Give the extent of all Trypanosoma brucei.
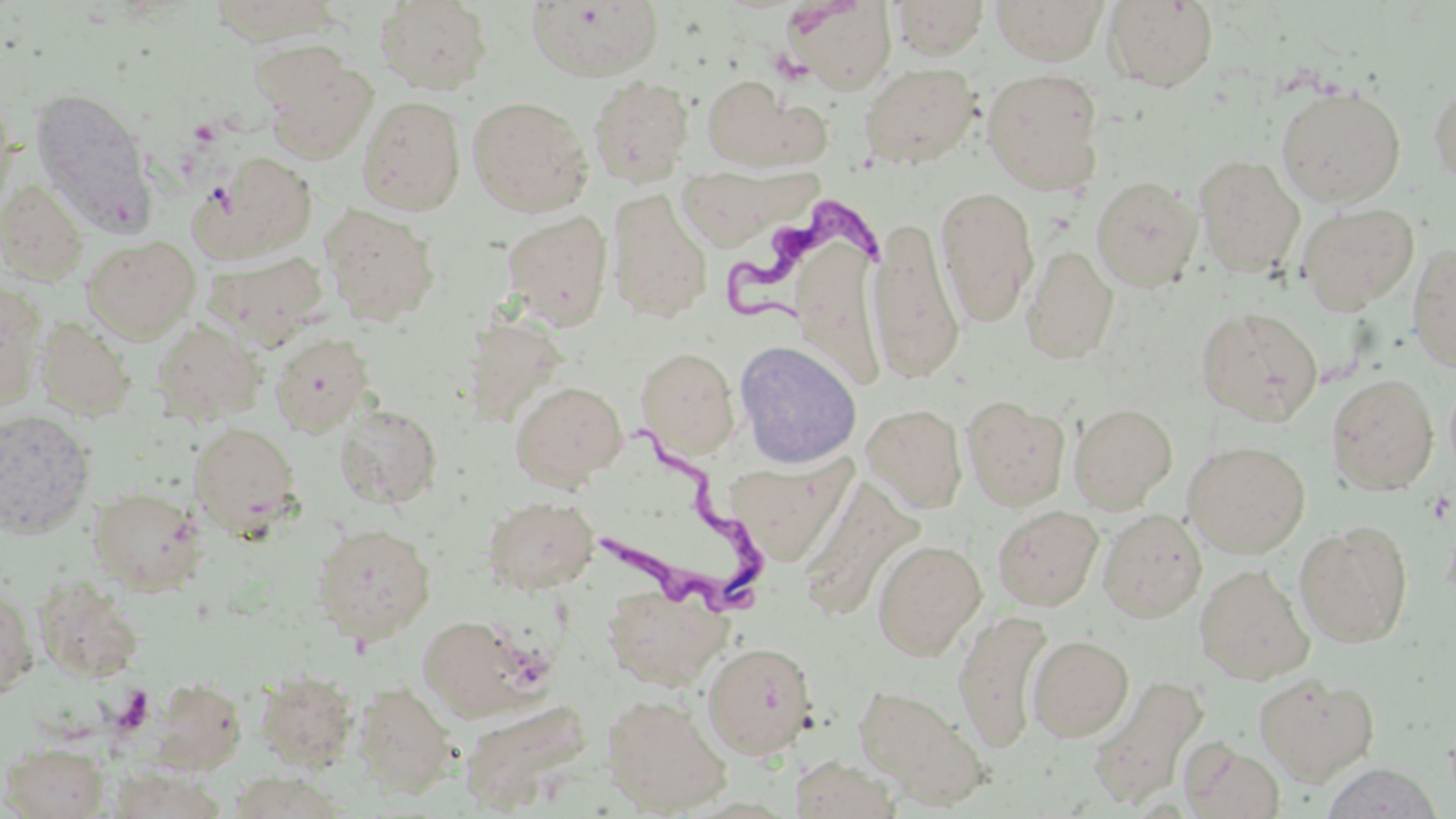
Approximate bounding boxes as named x1/y1/x2/y2 corners in pixels.
Trypanosoma brucei: (x1=719, y1=196, x2=880, y2=326), (x1=591, y1=423, x2=774, y2=619).

Uninfected red blood cell locations: (x1=206, y1=0, x2=344, y2=45), (x1=787, y1=0, x2=896, y2=94), (x1=991, y1=0, x2=1108, y2=64), (x1=375, y1=1, x2=493, y2=93), (x1=527, y1=1, x2=664, y2=82), (x1=890, y1=1, x2=989, y2=60), (x1=1104, y1=1, x2=1219, y2=91), (x1=258, y1=47, x2=378, y2=161), (x1=858, y1=62, x2=982, y2=170), (x1=982, y1=69, x2=1106, y2=196), (x1=588, y1=75, x2=695, y2=186), (x1=700, y1=75, x2=826, y2=172), (x1=1428, y1=80, x2=1456, y2=189), (x1=0, y1=85, x2=18, y2=212), (x1=1274, y1=85, x2=1406, y2=206), (x1=29, y1=86, x2=154, y2=230), (x1=357, y1=95, x2=467, y2=215), (x1=467, y1=96, x2=594, y2=217), (x1=195, y1=150, x2=318, y2=260), (x1=1193, y1=154, x2=1305, y2=278), (x1=681, y1=163, x2=824, y2=255), (x1=1091, y1=175, x2=1203, y2=292), (x1=0, y1=178, x2=89, y2=285), (x1=935, y1=186, x2=1039, y2=327), (x1=605, y1=189, x2=713, y2=323), (x1=1297, y1=202, x2=1419, y2=315), (x1=320, y1=203, x2=441, y2=325), (x1=500, y1=210, x2=613, y2=329), (x1=868, y1=216, x2=965, y2=384), (x1=83, y1=235, x2=201, y2=343), (x1=794, y1=235, x2=887, y2=392), (x1=1407, y1=243, x2=1456, y2=372), (x1=1021, y1=244, x2=1119, y2=365), (x1=206, y1=249, x2=327, y2=346), (x1=1, y1=281, x2=47, y2=410), (x1=1196, y1=306, x2=1323, y2=426), (x1=35, y1=316, x2=136, y2=419), (x1=151, y1=319, x2=266, y2=424), (x1=270, y1=333, x2=373, y2=436), (x1=733, y1=339, x2=863, y2=470), (x1=636, y1=346, x2=740, y2=459), (x1=1326, y1=374, x2=1438, y2=495), (x1=510, y1=381, x2=627, y2=489), (x1=961, y1=395, x2=1071, y2=511), (x1=333, y1=402, x2=443, y2=509), (x1=1069, y1=402, x2=1177, y2=513), (x1=862, y1=403, x2=967, y2=512), (x1=0, y1=409, x2=96, y2=538), (x1=189, y1=421, x2=302, y2=535), (x1=1183, y1=441, x2=1310, y2=558), (x1=725, y1=456, x2=853, y2=566), (x1=797, y1=479, x2=926, y2=622), (x1=88, y1=487, x2=206, y2=594), (x1=482, y1=495, x2=598, y2=594), (x1=992, y1=505, x2=1103, y2=611), (x1=1097, y1=508, x2=1207, y2=622), (x1=1295, y1=520, x2=1413, y2=649), (x1=312, y1=522, x2=437, y2=644), (x1=873, y1=538, x2=986, y2=660), (x1=1194, y1=563, x2=1315, y2=685), (x1=33, y1=576, x2=145, y2=683), (x1=0, y1=580, x2=38, y2=701), (x1=604, y1=585, x2=732, y2=690), (x1=952, y1=608, x2=1053, y2=752), (x1=419, y1=615, x2=540, y2=720), (x1=1028, y1=634, x2=1134, y2=741), (x1=701, y1=640, x2=818, y2=759), (x1=255, y1=669, x2=359, y2=770), (x1=1088, y1=673, x2=1209, y2=808), (x1=1254, y1=673, x2=1379, y2=785), (x1=147, y1=678, x2=247, y2=776), (x1=353, y1=681, x2=457, y2=796), (x1=853, y1=685, x2=988, y2=804), (x1=603, y1=692, x2=732, y2=815), (x1=459, y1=697, x2=593, y2=813), (x1=1181, y1=739, x2=1286, y2=818), (x1=2, y1=742, x2=110, y2=818), (x1=791, y1=755, x2=901, y2=818), (x1=1321, y1=762, x2=1444, y2=819), (x1=106, y1=766, x2=228, y2=818), (x1=226, y1=771, x2=346, y2=818). Platelet locations: (x1=189, y1=119, x2=222, y2=149). Slide-level diagnosis: Trypanosoma brucei. Light microscopy. Image is 1456×819 pixels. May-Grünwald-Giemsa-stained preparation. Thin blood film. Captured at 1000x magnification. One field of a larger specimen.